Report the malaria status of this cell.
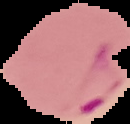
It is parasitized.

Summary:
  - Image type: cell region segmented out of the field of view; surrounding area masked to black
  - Preparation: thin blood film
  - Image size: 130×124 pixels